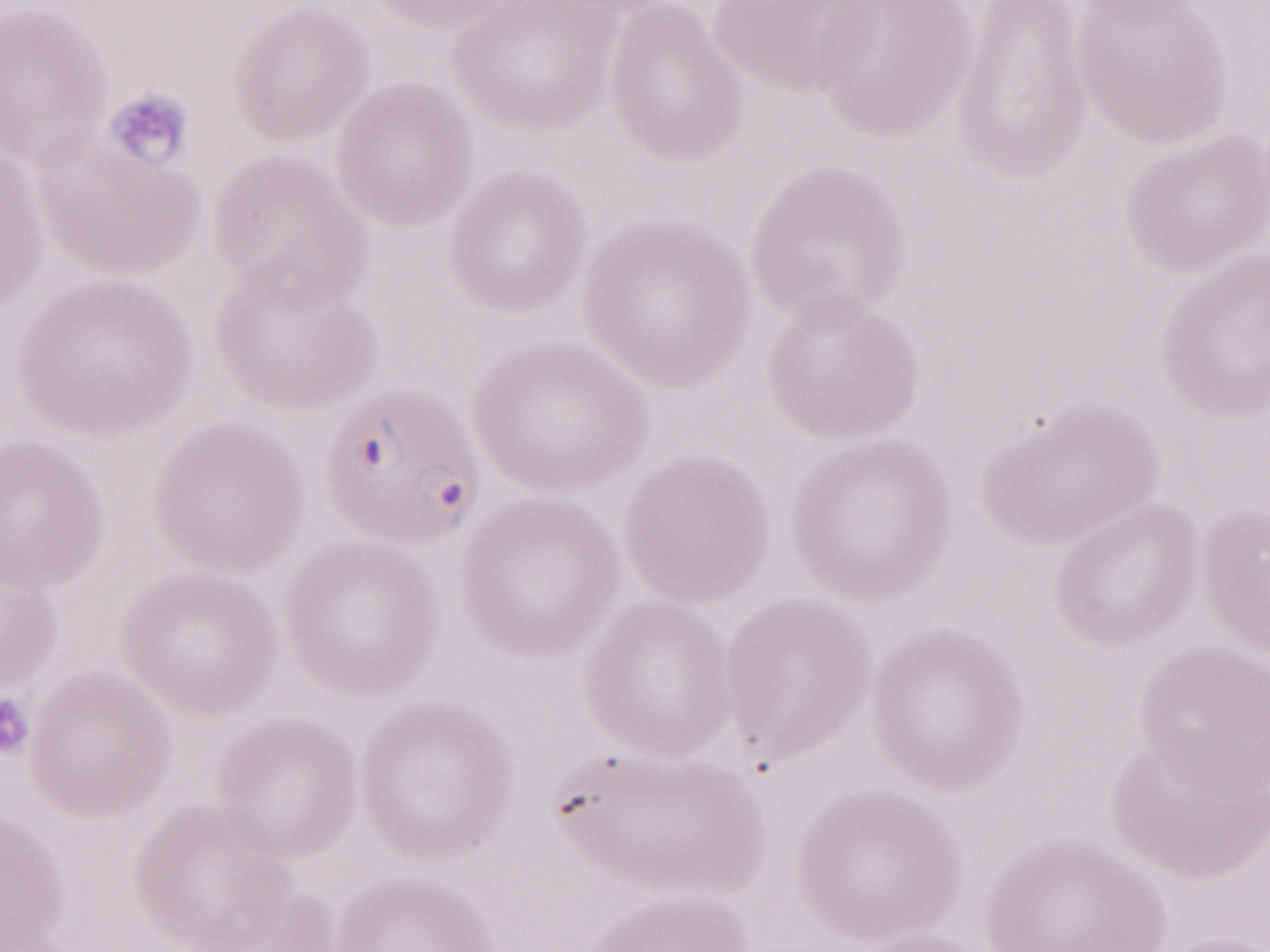

1,000x magnification. Patient-level malaria diagnosis: positive. Single field of view. Olympus BX43 microscope, Olympus DP73 camera. Image is 1270×952 pixels. Thin blood smear. May-Grünwald-Giemsa stain.